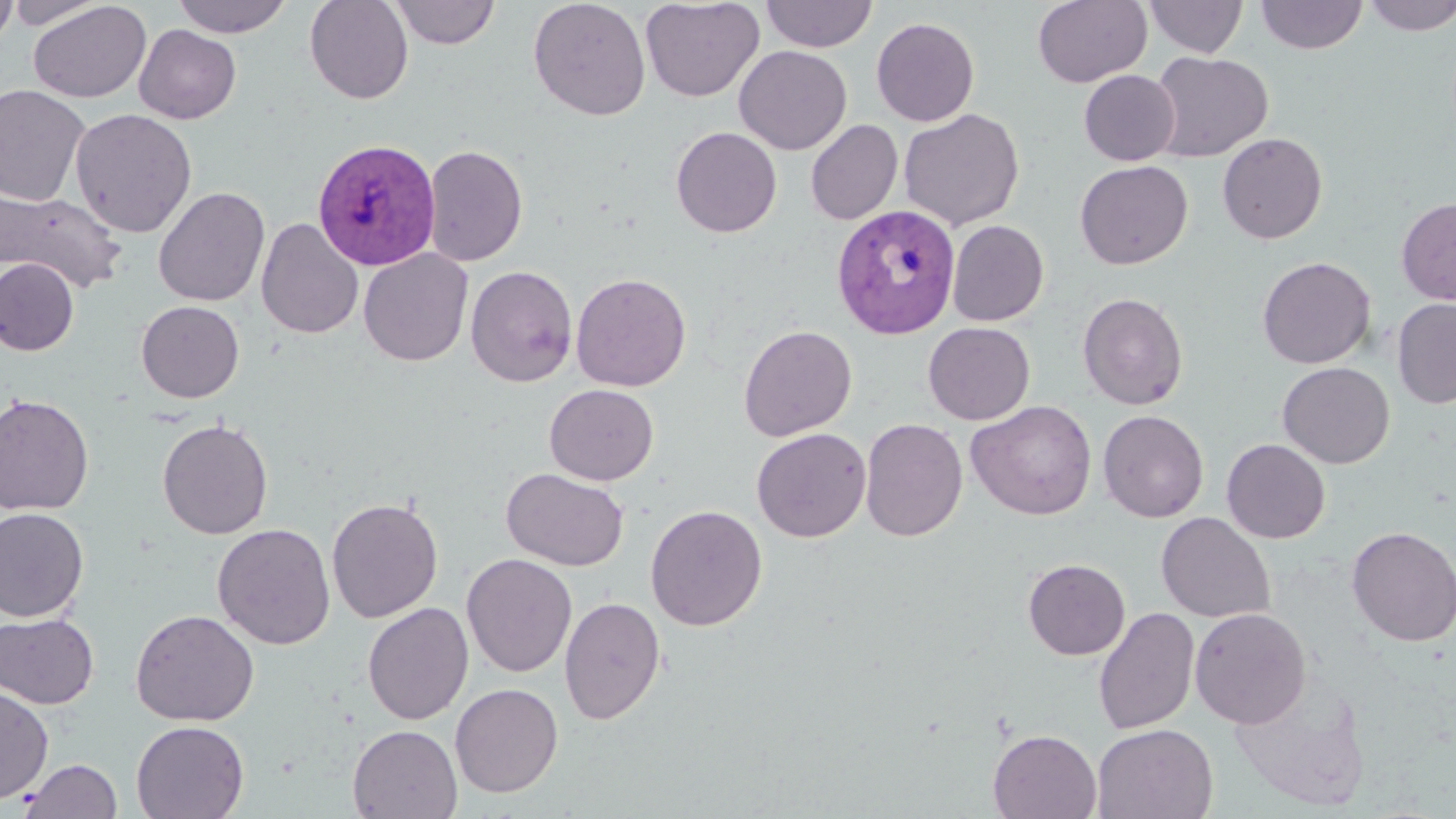

slide-level diagnosis = Plasmodium vivax
field of view = single
preparation = thin blood film
magnification = 1000x
image size = 1456×819 pixels
stain = May-Grünwald-Giemsa
Plasmodium vivax-infected red blood cell locations = approximate bounding boxes as (x1, y1, x2, y2) in pixels: (312, 137, 441, 270), (832, 203, 961, 340)
uninfected red blood cell locations = approximate bounding boxes as (x1, y1, x2, y2) in pixels: (0, 0, 18, 53), (4, 0, 111, 29), (27, 0, 151, 103), (171, 0, 294, 37), (304, 0, 413, 104), (389, 0, 500, 48), (528, 0, 651, 121), (641, 0, 765, 102), (760, 0, 879, 53), (1033, 0, 1151, 88), (1144, 0, 1248, 58), (1255, 0, 1368, 54), (1362, 0, 1456, 36), (871, 17, 980, 127), (134, 24, 241, 124), (734, 45, 852, 155), (1149, 51, 1273, 162), (1078, 69, 1180, 166), (0, 84, 91, 206), (70, 108, 197, 237), (898, 108, 1025, 230), (805, 120, 903, 225), (670, 127, 782, 237), (1217, 132, 1328, 243), (422, 143, 528, 267), (1074, 160, 1193, 270), (153, 186, 270, 306), (1, 188, 127, 294), (1396, 197, 1456, 305), (256, 218, 365, 339), (947, 220, 1049, 326), (358, 248, 473, 366), (1257, 256, 1376, 369), (0, 257, 79, 355), (465, 265, 578, 387), (571, 272, 692, 391), (1077, 292, 1189, 410), (1392, 298, 1456, 409), (136, 300, 245, 403), (923, 321, 1035, 425), (738, 324, 857, 441), (1277, 361, 1394, 468), (544, 383, 659, 485), (0, 393, 95, 515), (967, 400, 1097, 520), (1098, 410, 1208, 522), (157, 418, 273, 539), (859, 418, 968, 542), (751, 427, 871, 542), (1222, 439, 1331, 543), (501, 467, 629, 571), (326, 496, 444, 623), (645, 504, 767, 631), (0, 507, 90, 622), (1156, 512, 1276, 624), (212, 523, 335, 650), (1346, 526, 1456, 647), (461, 553, 577, 677), (1023, 558, 1130, 660), (559, 596, 666, 725), (362, 602, 473, 725), (1093, 607, 1199, 736), (1190, 607, 1310, 729), (130, 609, 260, 726), (1, 612, 99, 709), (1230, 674, 1371, 813), (450, 683, 563, 797), (0, 684, 54, 804), (131, 720, 249, 819), (1091, 723, 1218, 819), (347, 724, 463, 819), (987, 729, 1102, 818), (19, 758, 123, 818)
modality = light microscopy